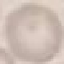 Result: negative for malaria parasites. Thin blood smear. Cell patch, automatically extracted from a larger field of view and resized to 64 × 64 pixels. Photographed with a smartphone camera at the microscope eyepiece. Giemsa-stained preparation.